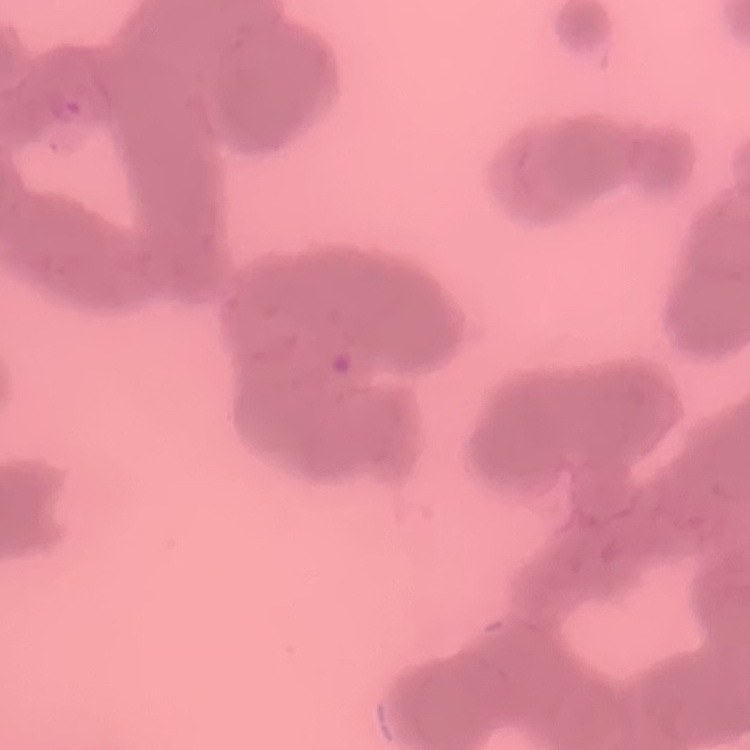

{
  "erythrocyte_morphology": "rouleaux formation",
  "stain": "Field's or Giemsa",
  "preparation": "thin blood film",
  "image_type": "one tile cut from a larger photomicrograph"
}